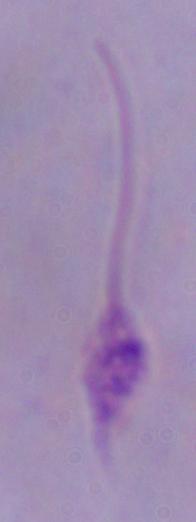

{
  "identification": "Leishmania",
  "modality": "micrograph",
  "magnification": "1000x"
}